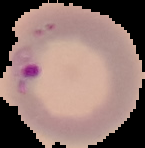
image size = 145×148 pixels
malaria status = parasitized
preparation = thin blood film
image type = cell region segmented out of the field of view; surrounding area masked to black